Name the parasite shown.
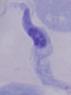

This is a trypanosome.

1000x magnification. Photomicrograph.